Comment on the morphology of the red blood cells.
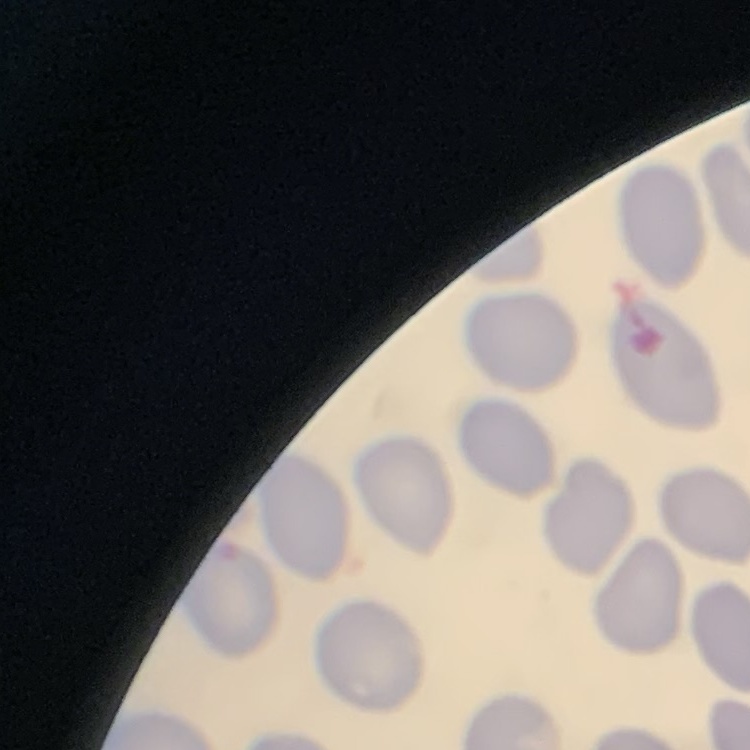

They show no rouleaux formation.

{
  "stain": "Field's or Giemsa",
  "preparation": "thin blood film",
  "image_type": "square crop of a larger photomicrograph"
}